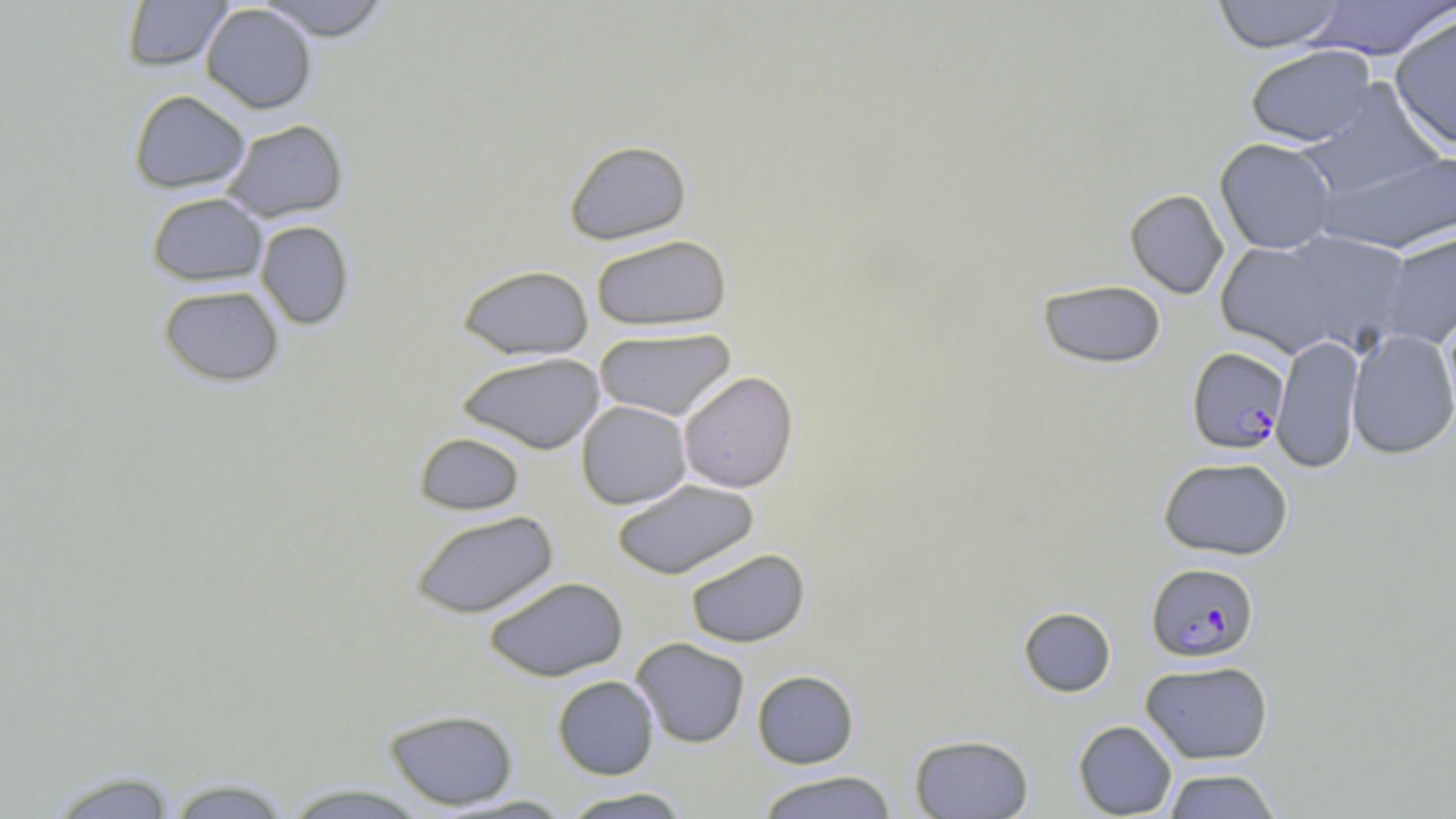

slide_level_diagnosis: Plasmodium falciparum
modality: light microscopy
stain: May-Grünwald-Giemsa
field_of_view: one of a larger specimen
preparation: thin blood smear
plasmodium_falciparum_infected_red_blood_cell_locations: 'approximate bounding boxes as (x1,y1)-(x2,y2) corner pairs in pixels: (1187,346)-(1290,454), (1146,562)-(1260,662)'
image_size: 1456×819 pixels
magnification: 1000x
uninfected_red_blood_cell_locations: 'approximate bounding boxes as (x1,y1)-(x2,y2) corner pairs in pixels: (121,0)-(233,72), (255,0)-(393,41), (1211,0)-(1347,53), (1304,1)-(1455,60), (200,4)-(317,114), (1390,12)-(1456,150), (1244,45)-(1376,146), (1300,81)-(1446,200), (128,89)-(251,193), (220,118)-(349,223), (563,138)-(692,245), (1214,138)-(1340,254), (1318,148)-(1456,255), (1124,189)-(1229,299), (146,192)-(268,286), (255,220)-(355,330), (1376,230)-(1456,349), (1215,233)-(1405,360), (590,234)-(732,332), (456,264)-(594,360), (1037,279)-(1167,369), (157,284)-(285,387), (1442,305)-(1456,425), (593,327)-(736,421), (1346,329)-(1456,459), (1271,335)-(1365,473), (456,352)-(605,454), (678,370)-(798,493), (575,400)-(692,509), (414,432)-(525,515), (1158,456)-(1294,560), (611,479)-(760,580), (410,510)-(559,619), (685,547)-(810,648), (483,576)-(629,681), (1018,606)-(1116,697), (631,638)-(750,748), (1140,660)-(1274,764), (751,669)-(860,768), (552,675)-(659,779), (383,709)-(518,810), (1073,720)-(1177,818), (909,733)-(1034,818), (1161,768)-(1282,818), (43,769)-(181,818), (754,770)-(899,818), (164,776)-(294,818), (277,783)-(432,818), (559,787)-(692,818), (444,794)-(576,817)'